Identify the cell.
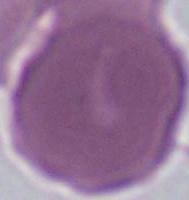
This is an erythrocyte.

magnification = 1000x
modality = micrograph